Locate every Plasmodium falciparum-infected red blood cell.
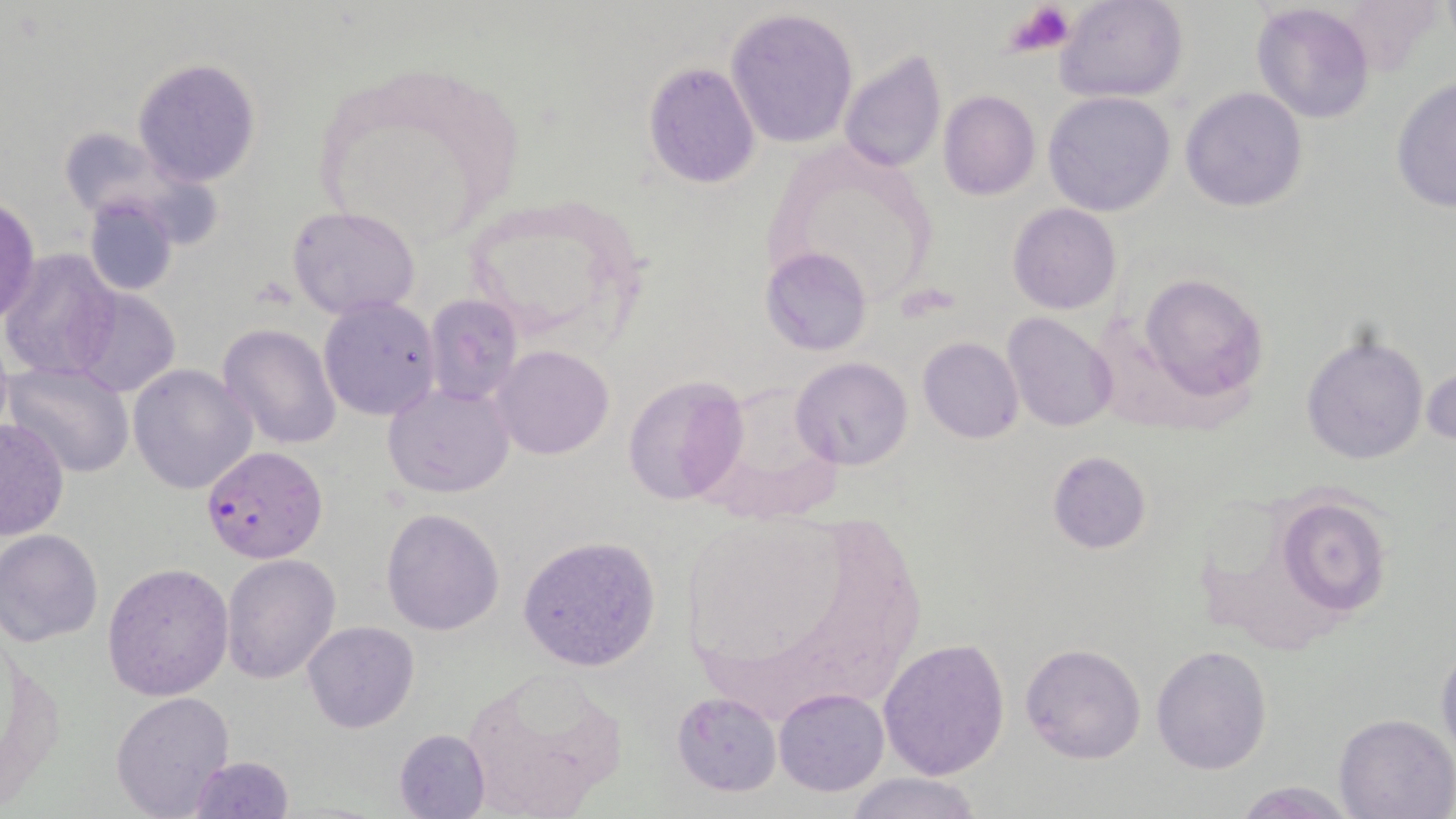
Approximate bounding boxes as (x1,y1)-(x2,y2) corner pairs in pixels.
Plasmodium falciparum-infected red blood cells: (201,445)-(328,563).

slide-level diagnosis = Plasmodium falciparum
magnification = 1000x
uninfected red blood cell locations = approximate bounding boxes as (x1,y1)-(x2,y2) corner pairs in pixels: (1053,0)-(1189,104), (1251,3)-(1377,123), (726,8)-(858,149), (836,48)-(947,176), (133,57)-(261,185), (643,62)-(760,188), (1390,78)-(1456,213), (1180,88)-(1308,211), (938,90)-(1041,200), (1042,91)-(1175,216), (83,194)-(179,296), (1,195)-(41,327), (455,196)-(647,347), (1008,204)-(1122,315), (287,205)-(422,319), (761,246)-(872,355), (1,250)-(120,381), (1138,272)-(1269,402), (67,288)-(181,398), (423,294)-(523,406), (317,297)-(440,421), (1004,314)-(1120,432), (218,323)-(342,450), (1300,327)-(1429,468), (917,336)-(1023,443), (491,345)-(615,459), (791,357)-(911,472), (5,359)-(132,479), (128,363)-(256,496), (1424,364)-(1455,449), (620,375)-(747,506), (383,382)-(514,499), (0,418)-(70,537), (1046,450)-(1151,553), (1276,495)-(1392,617), (381,508)-(505,634), (1,531)-(103,646), (517,534)-(663,671), (220,553)-(341,683), (102,562)-(234,700), (301,621)-(419,734), (877,637)-(1009,780), (1435,639)-(1456,767), (1019,642)-(1148,765), (1150,644)-(1273,773), (461,669)-(626,814), (112,689)-(236,816), (774,689)-(889,795), (670,691)-(781,796), (1333,713)-(1455,819), (392,728)-(490,819), (187,754)-(295,818), (844,773)-(985,819), (1233,780)-(1357,818)
platelet locations = approximate bounding boxes as (x1,y1)-(x2,y2) corner pairs in pixels: (1004,1)-(1073,60)
stain = May-Grünwald-Giemsa
image size = 1456×819 pixels
modality = optical microscopy
preparation = thin blood smear
field of view = single